Outline each blood parasite and name the species.
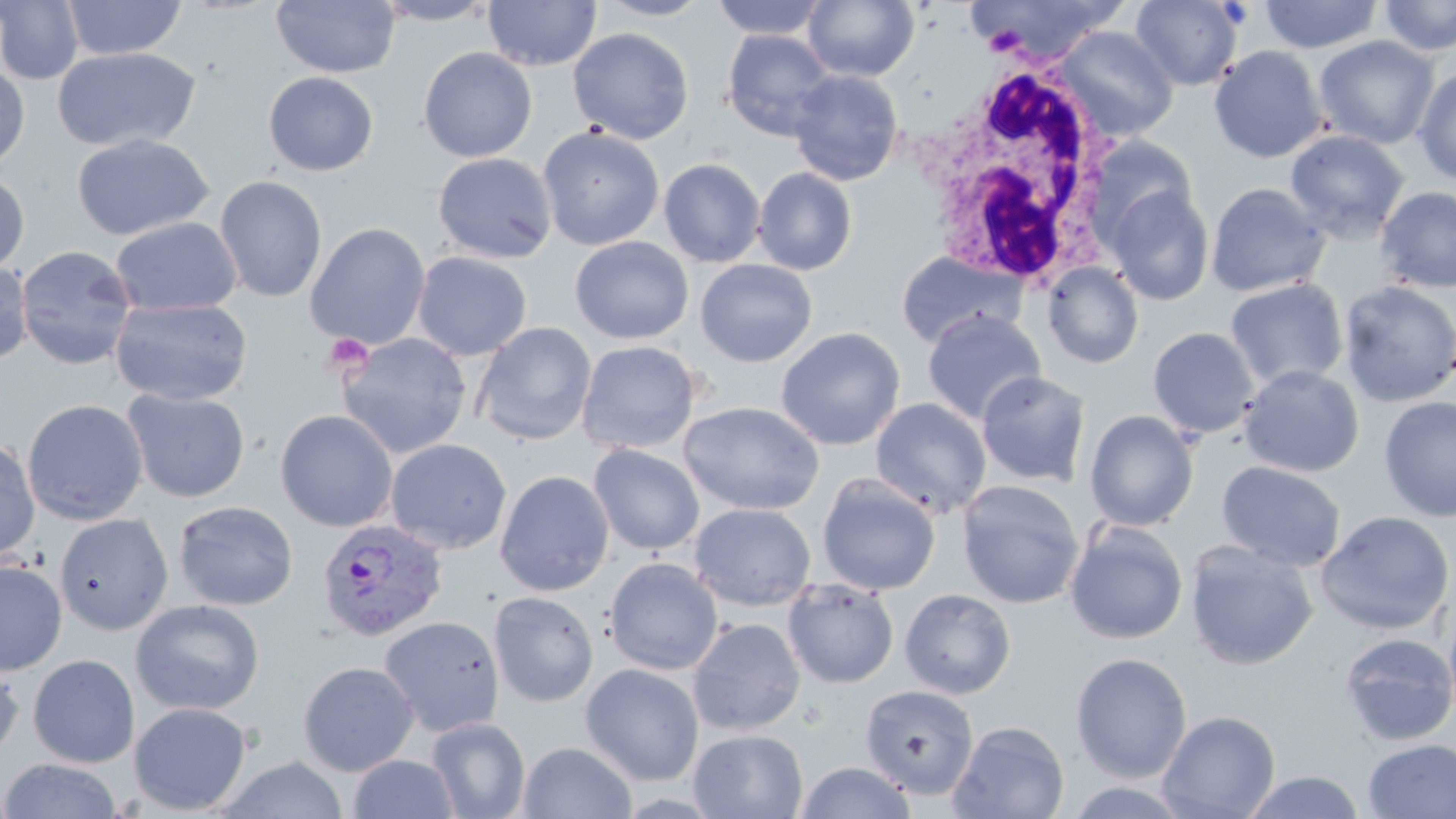

Approximate bounding boxes as (x1,y1)-(x2,y2) corner pairs in pixels.
Plasmodium vivax-infected red blood cells: (316,518)-(448,642).
No Plasmodium falciparum, Plasmodium ovale, Plasmodium malariae, Babesia divergens, or Trypanosoma brucei observed.

Summary:
  - Uninfected red blood cell locations: (0,0)-(85,85), (61,0)-(186,60), (270,0)-(400,78), (371,0)-(499,26), (484,0)-(601,71), (595,0)-(714,20), (709,0)-(830,39), (967,0)-(1127,66), (1130,0)-(1243,90), (1259,0)-(1384,54), (1378,0)-(1456,57), (804,1)-(919,82), (1054,26)-(1179,141), (567,27)-(695,144), (721,30)-(836,141), (1313,35)-(1440,150), (1208,45)-(1328,163), (51,46)-(202,153), (418,46)-(538,162), (0,61)-(30,173), (1413,66)-(1456,185), (788,69)-(903,186), (263,71)-(379,176), (538,125)-(665,252), (1285,129)-(1410,243), (71,133)-(213,241), (1084,134)-(1199,247), (433,152)-(557,263), (659,158)-(766,268), (752,167)-(857,275), (0,171)-(29,274), (214,176)-(327,303), (1206,182)-(1330,297), (1104,185)-(1214,306), (1374,186)-(1456,294), (110,216)-(242,316), (304,223)-(430,349), (570,236)-(694,344), (16,245)-(138,371), (895,251)-(1026,349), (412,252)-(532,361), (695,259)-(817,367), (0,260)-(33,366), (1042,261)-(1144,369), (1225,278)-(1348,391), (1337,280)-(1456,407), (110,298)-(252,406), (922,309)-(1045,425), (472,322)-(597,445), (1147,326)-(1260,439), (775,327)-(905,450), (336,332)-(472,459), (576,340)-(701,454), (1239,364)-(1364,478), (976,370)-(1091,487), (122,388)-(250,503), (1378,396)-(1456,523), (870,398)-(991,518), (22,399)-(148,526), (679,401)-(824,515), (275,409)-(398,532), (1084,409)-(1199,531), (385,438)-(512,554), (0,439)-(41,562), (588,444)-(705,555), (1216,461)-(1346,572), (495,470)-(614,596), (817,473)-(940,595), (956,480)-(1085,609), (173,500)-(299,611), (689,503)-(816,611), (1315,510)-(1455,635), (54,513)-(174,636), (1065,519)-(1188,645), (1184,540)-(1319,671), (604,556)-(723,675), (0,559)-(67,676), (783,579)-(900,689), (899,589)-(1015,699), (489,591)-(598,707), (1442,592)-(1456,729), (130,599)-(265,716), (378,616)-(504,736), (687,617)-(806,735), (1338,632)-(1456,746), (1070,652)-(1192,783), (0,654)-(24,764), (28,654)-(139,768), (298,661)-(419,777), (580,663)-(704,786), (860,685)-(979,800), (128,702)-(252,815), (1157,710)-(1281,819), (426,717)-(531,819), (948,720)-(1069,819), (689,728)-(809,819), (1362,738)-(1456,818), (518,741)-(637,819), (348,753)-(459,818), (217,756)-(349,819), (2,757)-(122,818), (795,761)-(917,819), (1240,769)-(1367,818)
  - White blood cell locations: (927,62)-(1123,291)
  - Platelet locations: (322,334)-(373,377)
  - Slide-level diagnosis: Plasmodium vivax
  - Magnification: 1000x
  - Field of view: one of a larger specimen
  - Image size: 1456×819 pixels
  - Preparation: thin blood smear
  - Stain: May-Grünwald-Giemsa
  - Modality: light microscopy